Describe the morphology of the red blood cells.
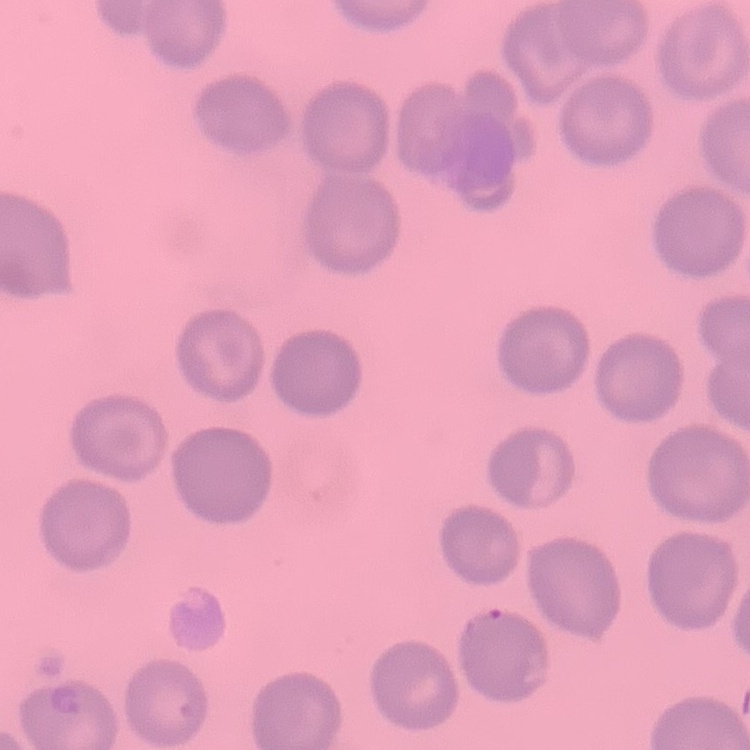

They show no rouleaux formation.

preparation = thin blood film
stain = Field's or Giemsa
image type = one tile cut from a larger photomicrograph